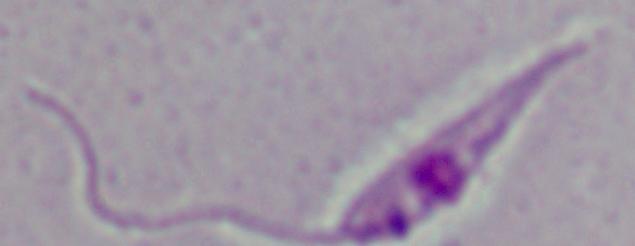

Summary:
  - Magnification: 1000x
  - Modality: photomicrograph
  - Identification: Leishmania